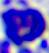

Captured at 400x magnification. A leukocyte is seen. Photomicrograph.